Assess this cell for malaria.
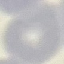

Uninfected.

preparation: thin blood film
image_type: automatically extracted cell patch, resized to 64 × 64 pixels
stain: Giemsa
capture: smartphone through the microscope eyepiece